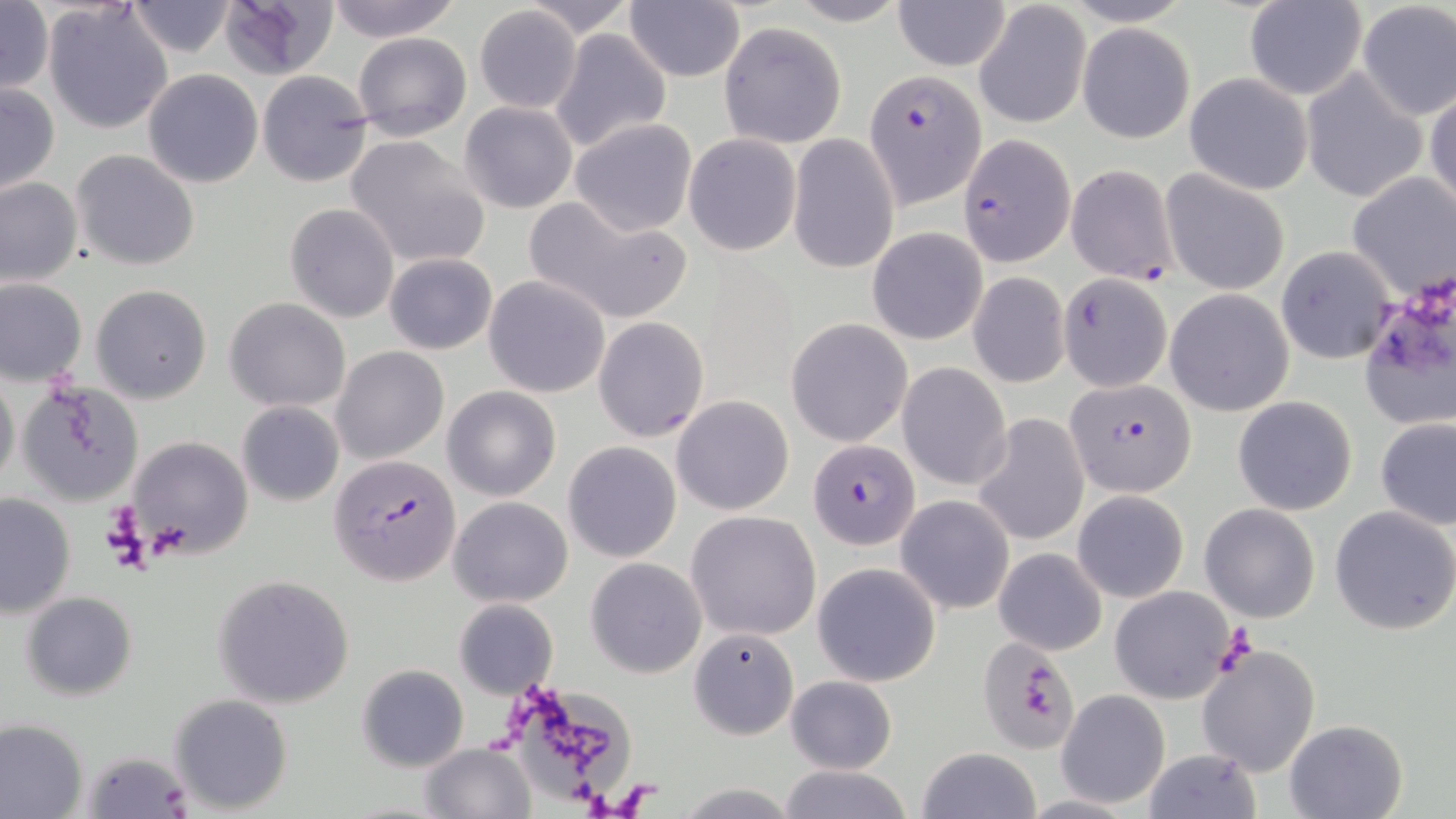

slide-level diagnosis = Plasmodium falciparum
platelet locations = approximate bounding boxes as (x1, y1, x2, y2) in pixels: (1214, 625, 1259, 673)
Plasmodium falciparum-infected red blood cell locations = approximate bounding boxes as (x1, y1, x2, y2) in pixels: (868, 67, 984, 208), (959, 135, 1076, 266), (1066, 164, 1178, 284), (1066, 379, 1197, 497), (808, 438, 919, 548), (328, 451, 462, 588)
stain = May-Grünwald-Giemsa
field of view = single
image size = 1456×819 pixels
magnification = 1000x
uninfected red blood cell locations = approximate bounding boxes as (x1, y1, x2, y2) in pixels: (217, 0, 339, 79), (324, 0, 462, 43), (517, 0, 640, 36), (783, 0, 912, 27), (892, 0, 1011, 72), (624, 1, 746, 82), (1243, 1, 1367, 99), (0, 2, 53, 92), (125, 2, 240, 58), (43, 3, 175, 134), (1355, 3, 1454, 122), (976, 4, 1090, 128), (473, 5, 582, 114), (719, 22, 847, 148), (1078, 23, 1194, 144), (549, 29, 672, 154), (352, 31, 472, 141), (142, 69, 265, 188), (257, 70, 373, 187), (1300, 70, 1430, 201), (1183, 73, 1313, 195), (1, 82, 60, 196), (1426, 84, 1456, 217), (460, 101, 576, 213), (570, 118, 697, 236), (684, 132, 801, 256), (787, 134, 900, 275), (345, 135, 490, 269), (72, 150, 201, 270), (1162, 169, 1289, 294), (1346, 173, 1456, 299), (0, 176, 82, 287), (524, 195, 693, 325), (285, 203, 398, 323), (868, 227, 987, 345), (1275, 246, 1395, 363), (384, 253, 497, 355), (968, 272, 1070, 388), (1058, 274, 1172, 394), (484, 275, 610, 398), (1, 279, 87, 386), (91, 284, 213, 404), (1164, 290, 1294, 416), (1359, 294, 1453, 429), (224, 297, 351, 411), (786, 317, 912, 447), (594, 318, 708, 442), (331, 347, 448, 465), (898, 363, 1011, 488), (0, 367, 20, 490), (17, 381, 144, 506), (443, 385, 561, 501), (672, 394, 795, 515), (1233, 395, 1359, 516), (236, 401, 344, 506), (972, 413, 1089, 547), (1375, 416, 1456, 529), (129, 435, 253, 560), (563, 440, 682, 562), (1074, 491, 1187, 601), (0, 492, 74, 620), (897, 494, 1014, 614), (448, 495, 573, 607), (1200, 503, 1321, 623), (1330, 505, 1456, 634), (686, 510, 822, 641), (993, 547, 1107, 655), (585, 558, 706, 678), (813, 562, 941, 686), (212, 574, 355, 707), (1107, 586, 1235, 704), (21, 591, 137, 700), (452, 598, 558, 699), (688, 627, 798, 739), (979, 637, 1080, 753), (1197, 645, 1322, 777), (356, 663, 470, 772), (786, 674, 897, 774), (501, 677, 636, 812), (1056, 689, 1170, 809), (168, 692, 294, 812), (0, 719, 87, 819), (1283, 719, 1407, 819), (417, 742, 536, 819), (915, 747, 1041, 819), (1143, 749, 1263, 816), (83, 750, 192, 817), (774, 764, 914, 819), (671, 784, 802, 817)
preparation = thin blood smear
modality = light microscopy